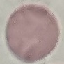

Result: negative for malaria parasites. Photographed with a smartphone camera at the microscope eyepiece. Giemsa-stained preparation. Cell patch, automatically extracted from a larger field of view and resized to 64 × 64 pixels. Thin blood film.